Give a bounding box for every parasitised red blood cell.
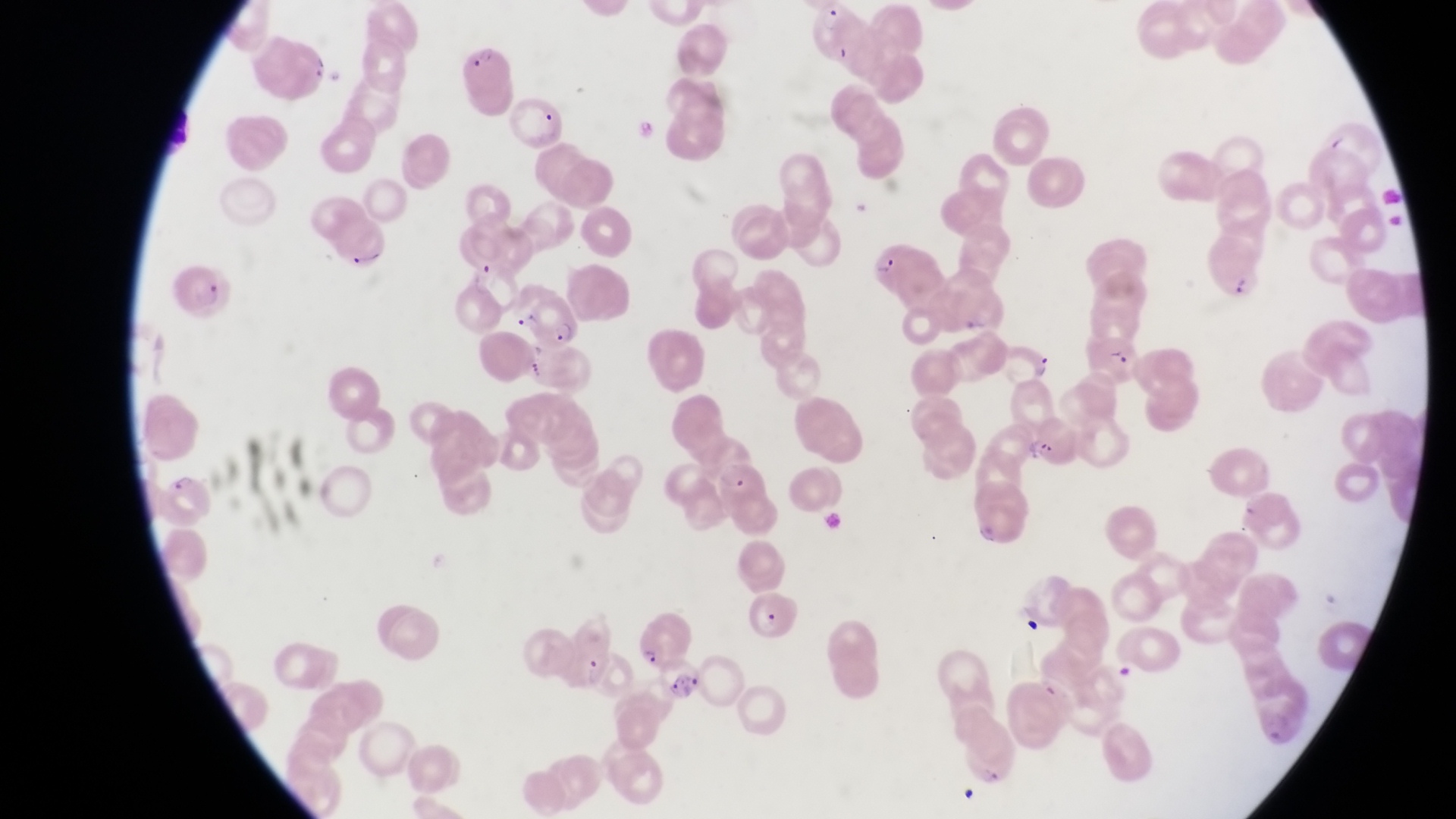

Approximate bounding boxes as [left, top, right, bottom] in pixels.
Parasitised red blood cells: [808, 6, 868, 66], [452, 42, 513, 98], [867, 237, 944, 308], [1200, 245, 1261, 303], [168, 261, 229, 321], [525, 287, 585, 351], [1086, 333, 1142, 389], [993, 338, 1052, 387], [714, 459, 769, 504], [153, 465, 208, 528], [746, 587, 805, 643], [632, 626, 688, 668].

image size = 1456×819 pixels
preparation = thin blood smear
field of view = single
magnification = 1000x
artifact (platelet-like body, stain precipitate, or debris) locations = approximate bounding boxes as [left, top, right, bottom] in pixels: [303, 52, 329, 85], [346, 243, 386, 272], [1036, 435, 1056, 461], [1018, 608, 1050, 640], [957, 777, 984, 804]
capture = smartphone photograph through the eyepiece of an Olympus CX-23 microscope
country = Uganda